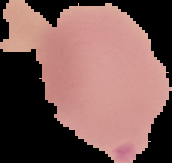

Result: Plasmodium parasites detected. Cell region segmented out of the field of view; the surrounding area is masked to black. Image is 172×163 pixels. From a thin blood film.